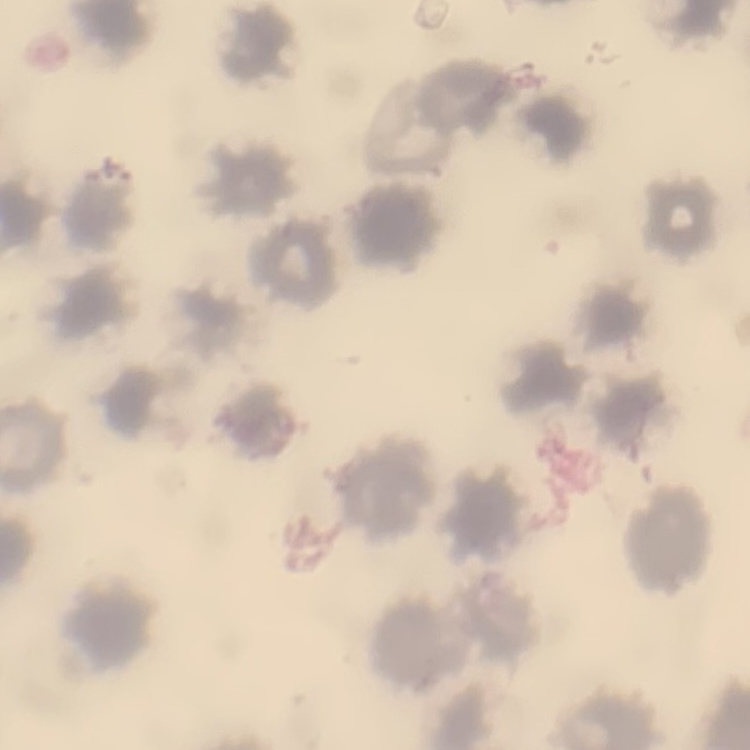
red blood cell morphology = no rouleaux formation
preparation = thin peripheral smear
image type = one tile cut from a larger photomicrograph
stain = Field's or Giemsa